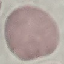
Summary:
  - Malaria status: uninfected
  - Capture: smartphone through the microscope eyepiece
  - Stain: Giemsa
  - Image type: cell patch, automatically extracted from a larger field of view and resized to 64 × 64 pixels
  - Preparation: thin blood smear